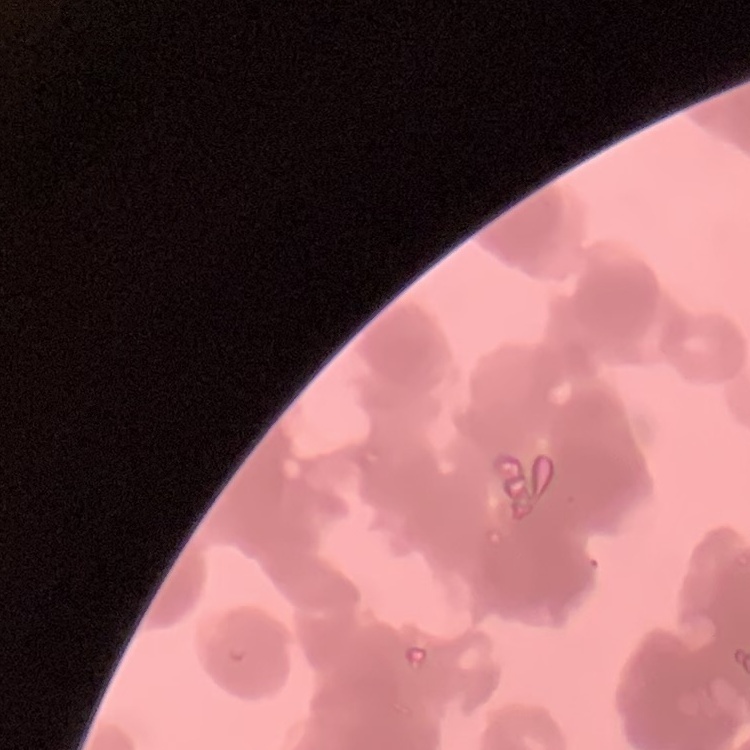
erythrocyte_morphology: rouleaux formation
stain: Field's or Giemsa
preparation: thin peripheral smear
image_type: one tile cut from a larger photomicrograph